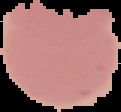
From a thin blood film. The area outside the segmented cell region is set to black. Result: no malaria parasites detected. Image is 121×112 pixels.